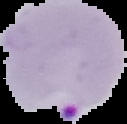
Malaria status: parasitized. Image is 127×124 pixels. From a thin blood film. The area outside the segmented cell region is set to black.